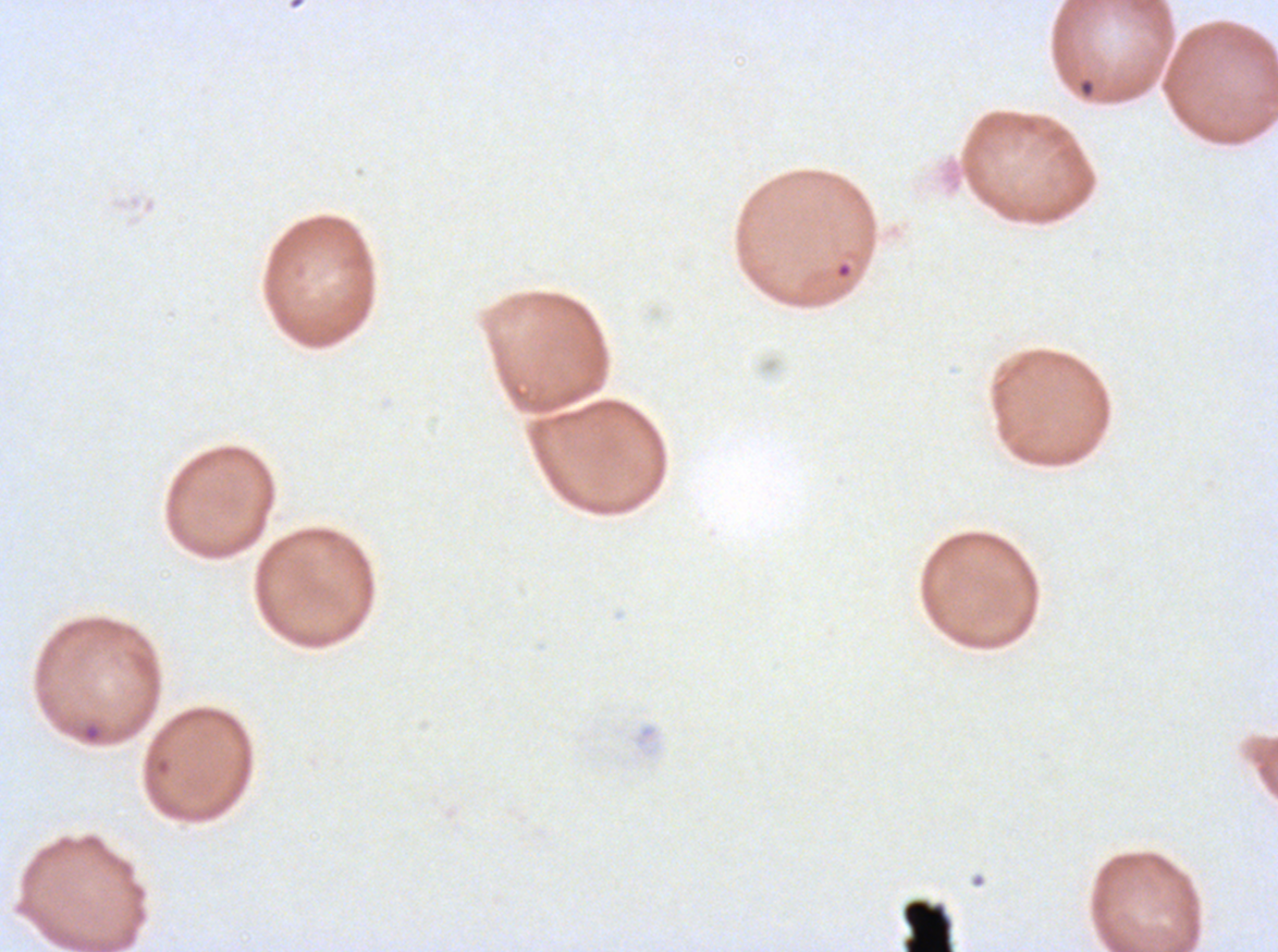

Approximate bounding rectangles given as corner coordinates in pixels from the top-left.
Summary:
  - Ring locations: (x1=1078, y1=78, x2=1095, y2=98), (x1=80, y1=720, x2=104, y2=744)
  - Debris locations: (x1=902, y1=898, x2=954, y2=951)
  - Image size: 1278×952 pixels
  - Field of view: sub-image separated from a larger composite
  - Stain: Giemsa
  - Specimen: ex-vivo P. falciparum culture from a patient in The Gambia, grown for 24 to 48 hours
  - Preparation: thin blood smear